Point out each Plasmodium parasite and each leukocyte.
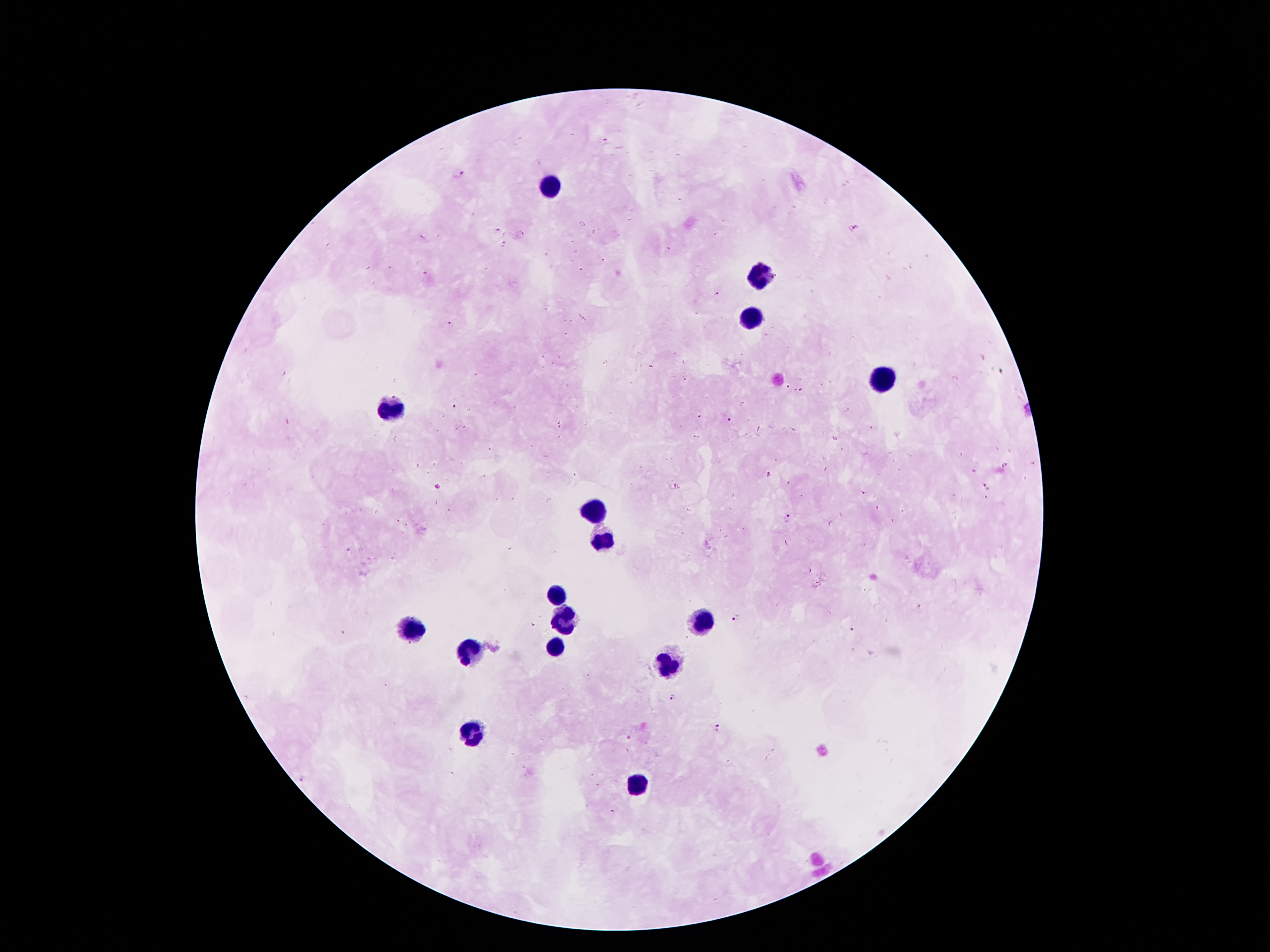

Approximate object centers, in pixels from the top-left corner.
Plasmodium parasites: (x=460, y=174), (x=853, y=229), (x=495, y=230), (x=506, y=245), (x=425, y=272), (x=718, y=294), (x=449, y=323), (x=454, y=407), (x=700, y=418), (x=729, y=419), (x=1032, y=464), (x=1005, y=466), (x=770, y=473), (x=789, y=482), (x=438, y=486), (x=987, y=486), (x=864, y=493), (x=987, y=499), (x=787, y=518), (x=398, y=521), (x=406, y=524), (x=348, y=550), (x=735, y=618), (x=674, y=697), (x=717, y=728).
Leukocytes: (x=547, y=185), (x=761, y=274), (x=745, y=319), (x=881, y=378), (x=388, y=412), (x=595, y=512), (x=602, y=537), (x=556, y=594), (x=697, y=621), (x=563, y=623), (x=411, y=626), (x=477, y=651), (x=556, y=653), (x=665, y=667), (x=472, y=732), (x=638, y=782).

Summary:
  - Image size: 1270×952 pixels
  - Field of view: one from this slide
  - Preparation: thick blood film
  - Capture: smartphone through the microscope eyepiece
  - Magnification: 100x
  - Patient malaria status: infected with Plasmodium falciparum
  - Stain: Giemsa